Locate every Trypanosoma brucei.
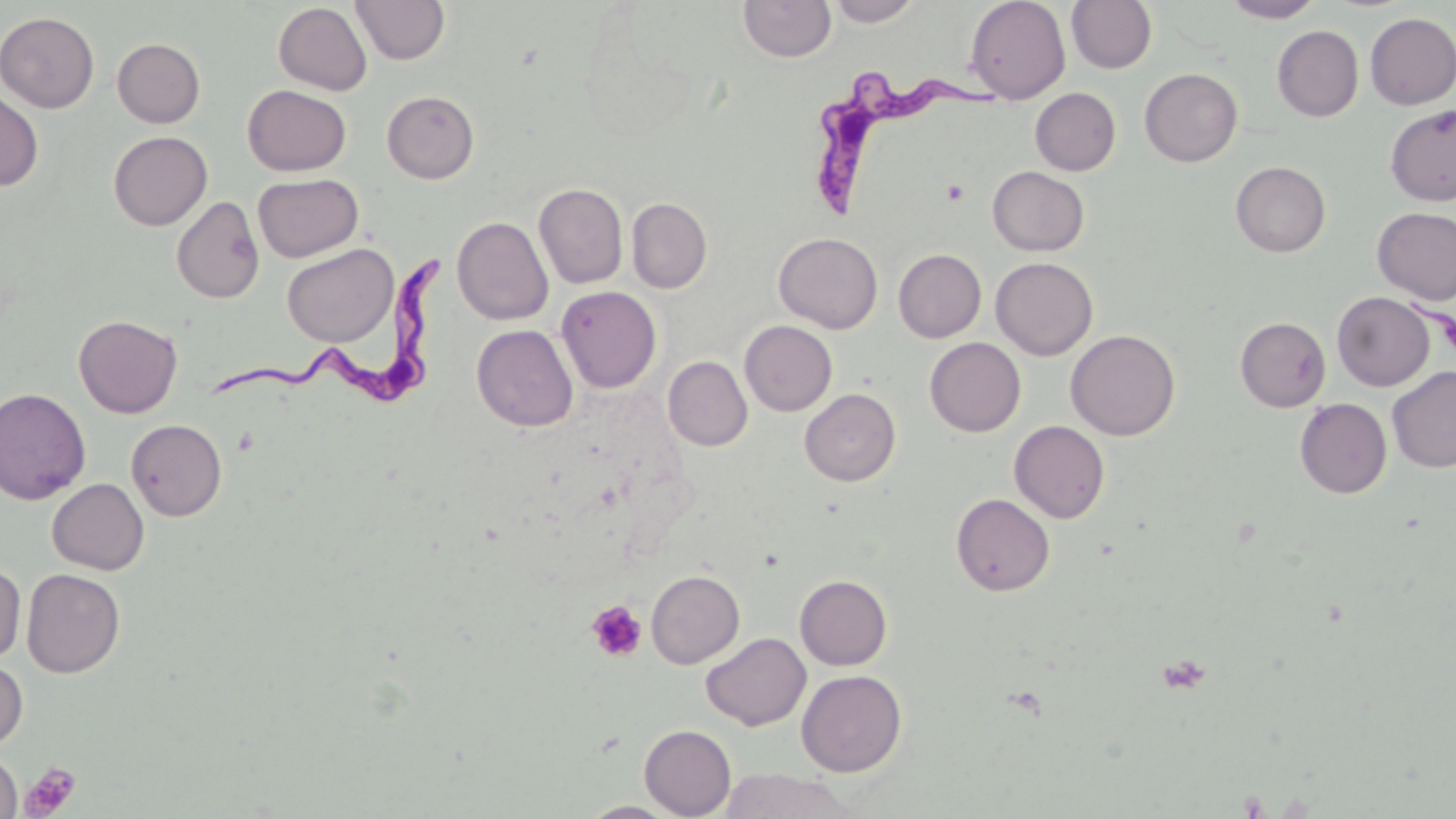
Approximate bounding boxes as named x1/y1/x2/y2 corners in pixels.
Trypanosoma brucei: (x1=808, y1=74, x2=1014, y2=225), (x1=210, y1=246, x2=458, y2=415).

slide_level_diagnosis: Trypanosoma brucei
field_of_view: one of a larger specimen
magnification: 1000x
modality: light microscopy
uninfected_red_blood_cell_locations: 'approximate bounding boxes as named x1/y1/x2/y2 corners in pixels: (x1=351, y1=0, x2=450, y2=65), (x1=825, y1=0, x2=922, y2=26), (x1=965, y1=0, x2=1070, y2=103), (x1=1066, y1=0, x2=1157, y2=73), (x1=1221, y1=0, x2=1325, y2=22), (x1=738, y1=1, x2=836, y2=62), (x1=273, y1=3, x2=372, y2=95), (x1=0, y1=12, x2=100, y2=113), (x1=1364, y1=13, x2=1456, y2=110), (x1=1272, y1=25, x2=1363, y2=121), (x1=112, y1=38, x2=205, y2=127), (x1=1139, y1=68, x2=1242, y2=167), (x1=243, y1=85, x2=351, y2=175), (x1=1030, y1=88, x2=1121, y2=175), (x1=0, y1=89, x2=43, y2=191), (x1=382, y1=90, x2=479, y2=183), (x1=1385, y1=104, x2=1456, y2=206), (x1=108, y1=131, x2=212, y2=230), (x1=1230, y1=161, x2=1331, y2=257), (x1=987, y1=166, x2=1089, y2=256), (x1=253, y1=173, x2=363, y2=262), (x1=533, y1=183, x2=628, y2=289), (x1=171, y1=196, x2=264, y2=303), (x1=627, y1=198, x2=712, y2=293), (x1=1372, y1=207, x2=1456, y2=305), (x1=452, y1=216, x2=553, y2=325), (x1=774, y1=232, x2=883, y2=333), (x1=281, y1=243, x2=398, y2=347), (x1=893, y1=249, x2=986, y2=342), (x1=991, y1=257, x2=1097, y2=360), (x1=556, y1=286, x2=661, y2=393), (x1=1332, y1=291, x2=1434, y2=391), (x1=73, y1=315, x2=182, y2=418), (x1=1235, y1=317, x2=1331, y2=411), (x1=740, y1=320, x2=837, y2=416), (x1=471, y1=324, x2=578, y2=432), (x1=1066, y1=330, x2=1180, y2=441), (x1=925, y1=337, x2=1025, y2=437), (x1=663, y1=356, x2=753, y2=451), (x1=1387, y1=366, x2=1456, y2=473), (x1=0, y1=388, x2=91, y2=505), (x1=799, y1=388, x2=901, y2=486), (x1=1294, y1=398, x2=1392, y2=499), (x1=126, y1=418, x2=227, y2=521), (x1=1009, y1=420, x2=1110, y2=523), (x1=47, y1=479, x2=148, y2=574), (x1=951, y1=493, x2=1054, y2=596), (x1=0, y1=563, x2=26, y2=664), (x1=21, y1=568, x2=125, y2=678), (x1=646, y1=570, x2=745, y2=668), (x1=795, y1=575, x2=892, y2=670), (x1=701, y1=632, x2=810, y2=731), (x1=0, y1=658, x2=28, y2=754), (x1=796, y1=669, x2=907, y2=777), (x1=639, y1=724, x2=736, y2=818), (x1=0, y1=752, x2=23, y2=817), (x1=716, y1=769, x2=860, y2=818), (x1=579, y1=801, x2=680, y2=818)'
stain: May-Grünwald-Giemsa
preparation: thin blood film
image_size: 1456×819 pixels
platelet_locations: 'approximate bounding boxes as named x1/y1/x2/y2 corners in pixels: (x1=941, y1=180, x2=969, y2=204), (x1=587, y1=600, x2=647, y2=662), (x1=20, y1=763, x2=81, y2=818)'